Assess this cell for malaria.
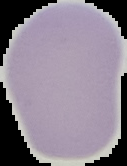
Uninfected.

Summary:
  - Preparation: thin blood film
  - Image size: 127×166 pixels
  - Image type: cell region segmented out of the field of view; surrounding area masked to black